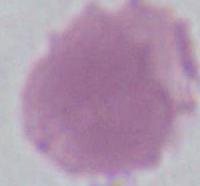

Photomicrograph. An erythrocyte is seen. 1000x magnification.